Outline each Plasmodium ovale-infected red blood cell.
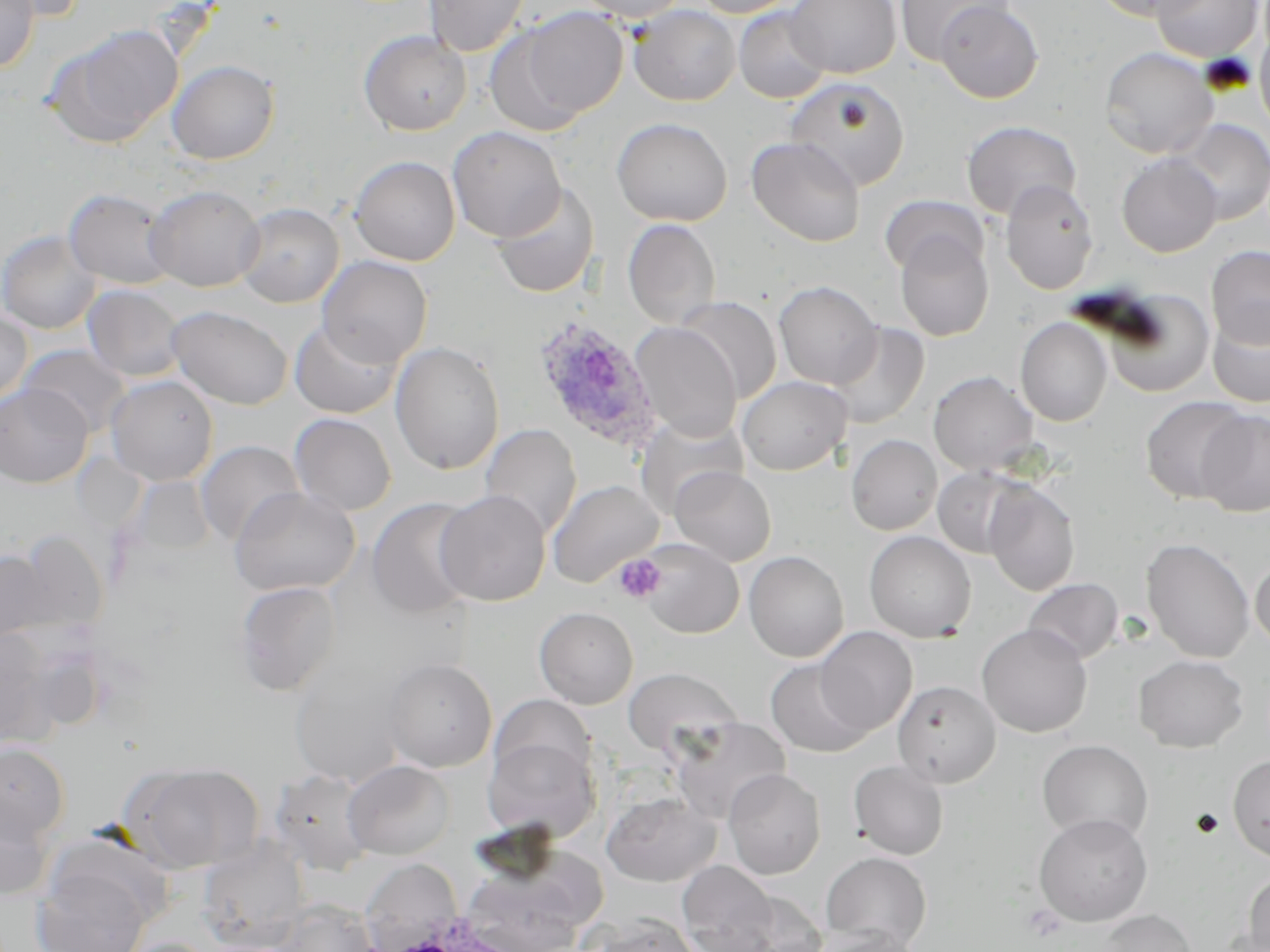

Approximate bounding boxes as (x1,y1)-(x2,y2) corner pairs in pixels.
Plasmodium ovale-infected red blood cells: (533,318)-(663,453).

Summary:
  - Uninfected red blood cell locations: (0,0)-(39,71), (2,0)-(90,22), (423,0)-(531,57), (575,0)-(689,22), (690,0)-(802,18), (786,0)-(901,78), (895,0)-(1013,66), (1090,0)-(1212,21), (1150,0)-(1265,63), (935,1)-(1044,103), (628,4)-(741,106), (505,5)-(629,127), (734,6)-(831,103), (1255,21)-(1270,135), (48,25)-(183,148), (358,30)-(471,135), (1099,46)-(1219,159), (167,60)-(279,164), (785,77)-(910,191), (611,117)-(732,226), (1172,119)-(1270,224), (962,120)-(1081,219), (447,126)-(566,242), (746,136)-(866,247), (1117,154)-(1221,257), (349,156)-(460,265), (1000,179)-(1099,295), (147,184)-(264,291), (492,184)-(599,298), (64,188)-(177,289), (879,195)-(989,277), (235,202)-(343,307), (622,219)-(720,328), (0,229)-(101,334), (894,231)-(994,341), (1205,245)-(1270,349), (316,255)-(432,368), (773,281)-(883,389), (83,285)-(185,382), (1102,289)-(1215,397), (678,297)-(781,404), (167,305)-(293,410), (0,309)-(32,405), (1208,309)-(1270,408), (1015,317)-(1112,426), (289,319)-(402,418), (630,322)-(742,441), (828,323)-(929,429), (390,342)-(504,474), (19,345)-(131,437), (928,371)-(1038,475), (105,375)-(218,485), (738,376)-(851,475), (0,384)-(92,488), (1140,396)-(1250,504), (1196,409)-(1270,517), (289,413)-(396,516), (635,415)-(747,517), (480,424)-(582,538), (846,434)-(942,535), (195,441)-(304,545), (933,465)-(1032,559), (670,466)-(776,566), (129,475)-(215,557), (548,480)-(663,587), (983,480)-(1079,596), (231,488)-(360,596), (435,490)-(551,606), (367,498)-(478,619), (864,530)-(977,642), (11,533)-(105,636), (1141,537)-(1255,663), (639,538)-(743,638), (0,549)-(59,642), (744,550)-(849,662), (1250,555)-(1270,652), (1023,578)-(1123,664), (235,581)-(342,695), (534,607)-(638,709), (976,623)-(1093,737), (814,627)-(917,736), (0,628)-(58,746), (1133,654)-(1249,752), (382,657)-(497,772), (289,659)-(411,788), (765,659)-(874,757), (623,667)-(742,759), (893,680)-(1001,787), (670,719)-(791,824), (482,735)-(600,842), (1037,740)-(1153,843), (0,741)-(70,843), (1228,755)-(1270,862), (342,760)-(453,860), (848,760)-(949,859), (126,761)-(262,873), (723,768)-(826,879), (270,769)-(376,873), (602,791)-(720,887), (0,795)-(56,901), (1034,813)-(1153,926), (197,838)-(310,951), (820,851)-(931,951), (458,852)-(601,952), (359,859)-(463,950), (677,860)-(780,951), (32,863)-(154,952), (1243,870)-(1270,951), (727,888)-(830,952), (272,899)-(380,952), (1094,909)-(1197,951), (589,914)-(701,952), (814,926)-(925,952), (113,937)-(221,952)
  - Platelet locations: (613,554)-(665,603), (1022,903)-(1067,942)
  - Slide-level diagnosis: Plasmodium ovale
  - Field of view: single
  - Magnification: 1000x
  - Modality: light microscopy
  - Image size: 1270×952 pixels
  - Preparation: thin blood smear
  - Stain: May-Grünwald-Giemsa